Locate every Plasmodium falciparum-infected red blood cell.
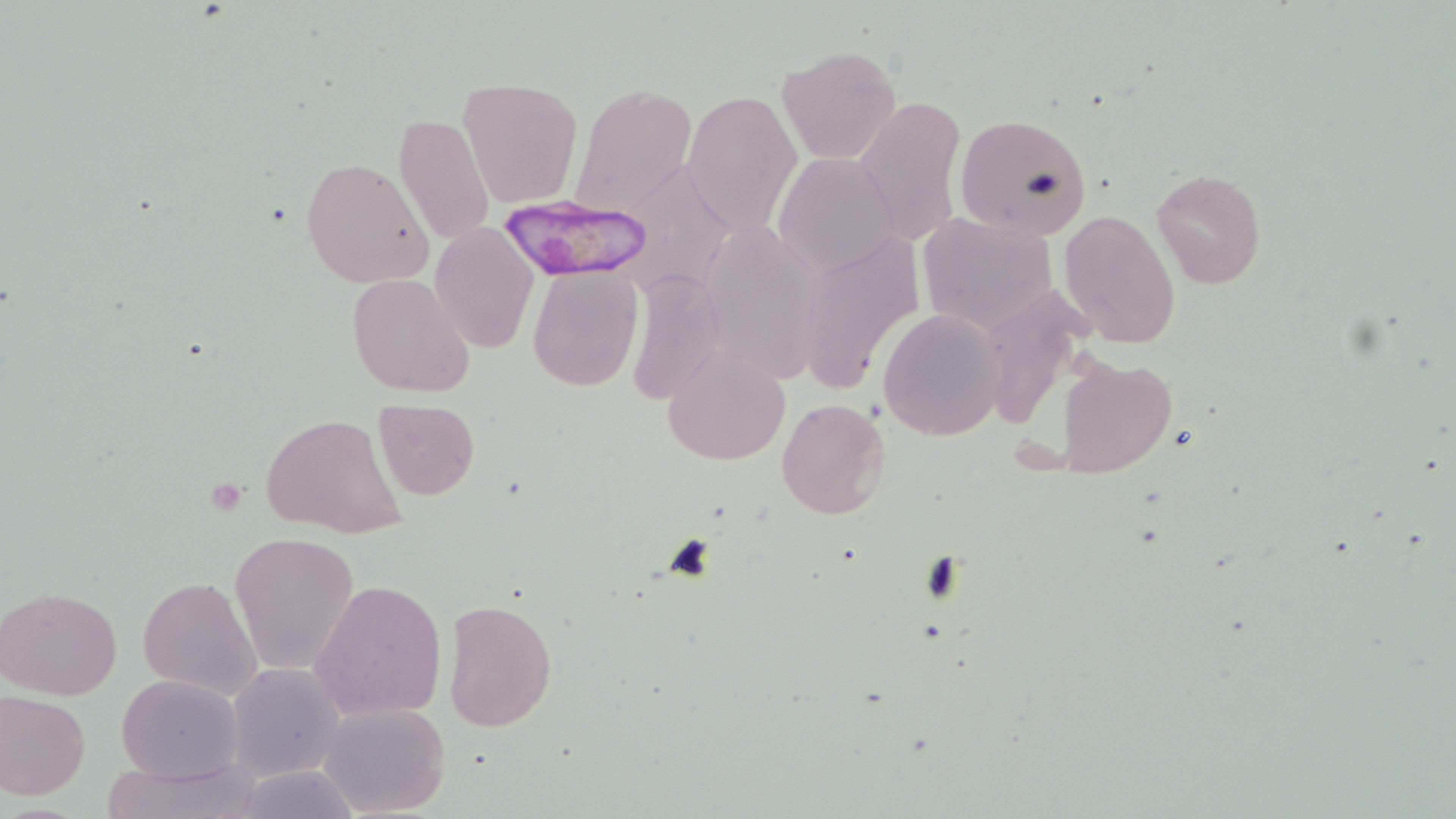
Approximate bounding boxes as (x1, y1, x2, y2) in pixels.
Plasmodium falciparum-infected red blood cells: (502, 197, 647, 283).

slide-level diagnosis = Plasmodium falciparum
field of view = one of a larger specimen
magnification = 1000x
modality = optical microscopy
image size = 1456×819 pixels
uninfected red blood cell locations = approximate bounding boxes as (x1, y1, x2, y2) in pixels: (777, 46, 903, 164), (458, 76, 584, 209), (572, 84, 697, 218), (682, 90, 800, 236), (851, 94, 967, 248), (394, 111, 495, 249), (954, 112, 1095, 240), (773, 150, 903, 277), (301, 155, 434, 289), (1151, 169, 1266, 291), (1058, 210, 1181, 349), (917, 211, 1059, 335), (430, 223, 539, 352), (800, 233, 924, 392), (530, 264, 641, 391), (347, 273, 474, 397), (878, 311, 1004, 440), (660, 344, 791, 468), (1053, 354, 1178, 480), (373, 398, 480, 499), (776, 398, 890, 520), (260, 413, 408, 541), (230, 531, 361, 674), (139, 575, 264, 703), (309, 578, 446, 723), (0, 585, 122, 700), (444, 599, 558, 734), (225, 663, 345, 782), (116, 674, 243, 783), (0, 689, 91, 801), (316, 700, 451, 818), (94, 759, 266, 819)
preparation = thin blood smear
stain = May-Grünwald-Giemsa